Assess this cell for malaria.
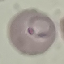
It is parasitized.

image type = cell patch, automatically extracted from a larger field of view and resized to 64 × 64 pixels
capture = smartphone camera at the microscope eyepiece
preparation = thin smear
stain = Giemsa